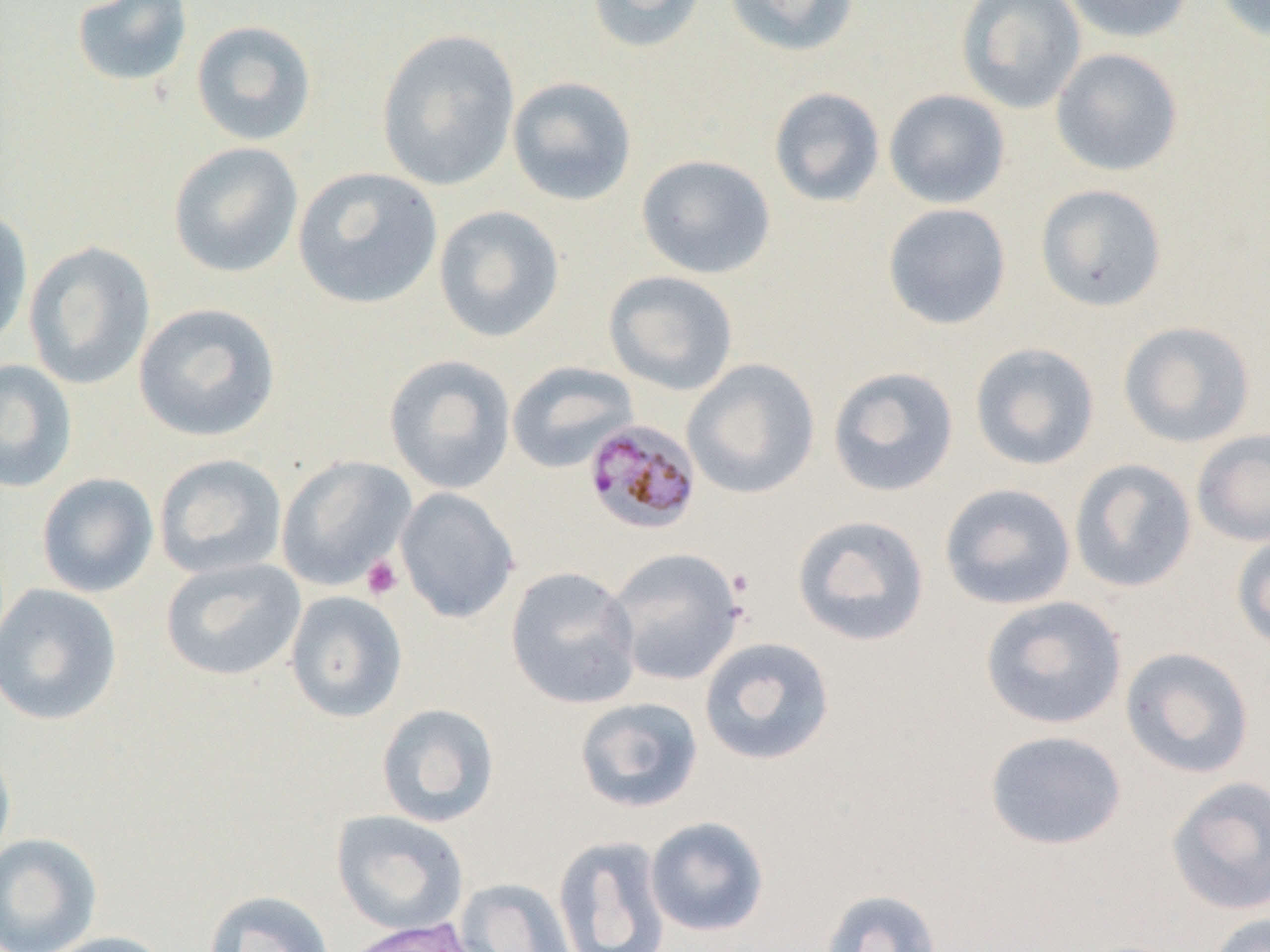
Approximate bounding boxes as (x1,y1)-(x2,y2) corner pairs in pixels. Platelet locations: (361,555)-(403,600). Uninfected red blood cell locations: (70,0)-(193,88), (585,0)-(707,54), (723,0)-(861,57), (955,0)-(1086,114), (1060,0)-(1195,44), (1212,0)-(1269,44), (190,19)-(317,147), (376,28)-(521,191), (1050,47)-(1184,176), (507,76)-(637,206), (769,87)-(885,207), (884,89)-(1011,209), (168,141)-(304,279), (636,154)-(776,279), (292,166)-(443,310), (1035,184)-(1167,312), (882,203)-(1012,330), (433,205)-(565,343), (0,206)-(33,350), (24,241)-(156,390), (603,270)-(739,397), (133,302)-(282,442), (1118,320)-(1256,448), (969,342)-(1100,471), (383,354)-(516,494), (682,358)-(821,500), (0,359)-(78,493), (506,361)-(639,473), (827,366)-(959,497), (1191,428)-(1270,547), (154,453)-(287,579), (275,456)-(417,591), (1069,458)-(1197,593), (37,472)-(159,598), (938,483)-(1077,610), (395,487)-(519,623), (792,514)-(930,647), (1230,530)-(1270,653), (605,547)-(746,686), (160,557)-(306,682), (506,566)-(642,709), (0,583)-(122,726), (284,590)-(408,723), (979,595)-(1128,730), (699,636)-(835,766), (1119,645)-(1255,779), (574,697)-(703,813), (376,703)-(500,827), (984,730)-(1127,850), (0,741)-(16,872), (1166,775)-(1270,916), (331,810)-(469,937), (645,816)-(769,937), (0,833)-(102,952), (552,835)-(671,952), (454,878)-(578,952), (820,887)-(942,952), (204,890)-(335,952), (1206,912)-(1270,952), (40,931)-(175,952). Plasmodium malariae-infected red blood cell locations: (583,419)-(701,536). Slide-level diagnosis: Plasmodium malariae. 1000x magnification. Thin blood smear. Image is 1270×952 pixels. One field of a larger specimen. Optical microscopy.